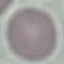

Summary:
  - Malaria status: uninfected
  - Stain: Giemsa
  - Preparation: thin blood smear
  - Image type: automatically extracted cell patch, resized to 64 × 64 pixels
  - Capture: smartphone through the microscope eyepiece